Outline every Plasmodium parasite.
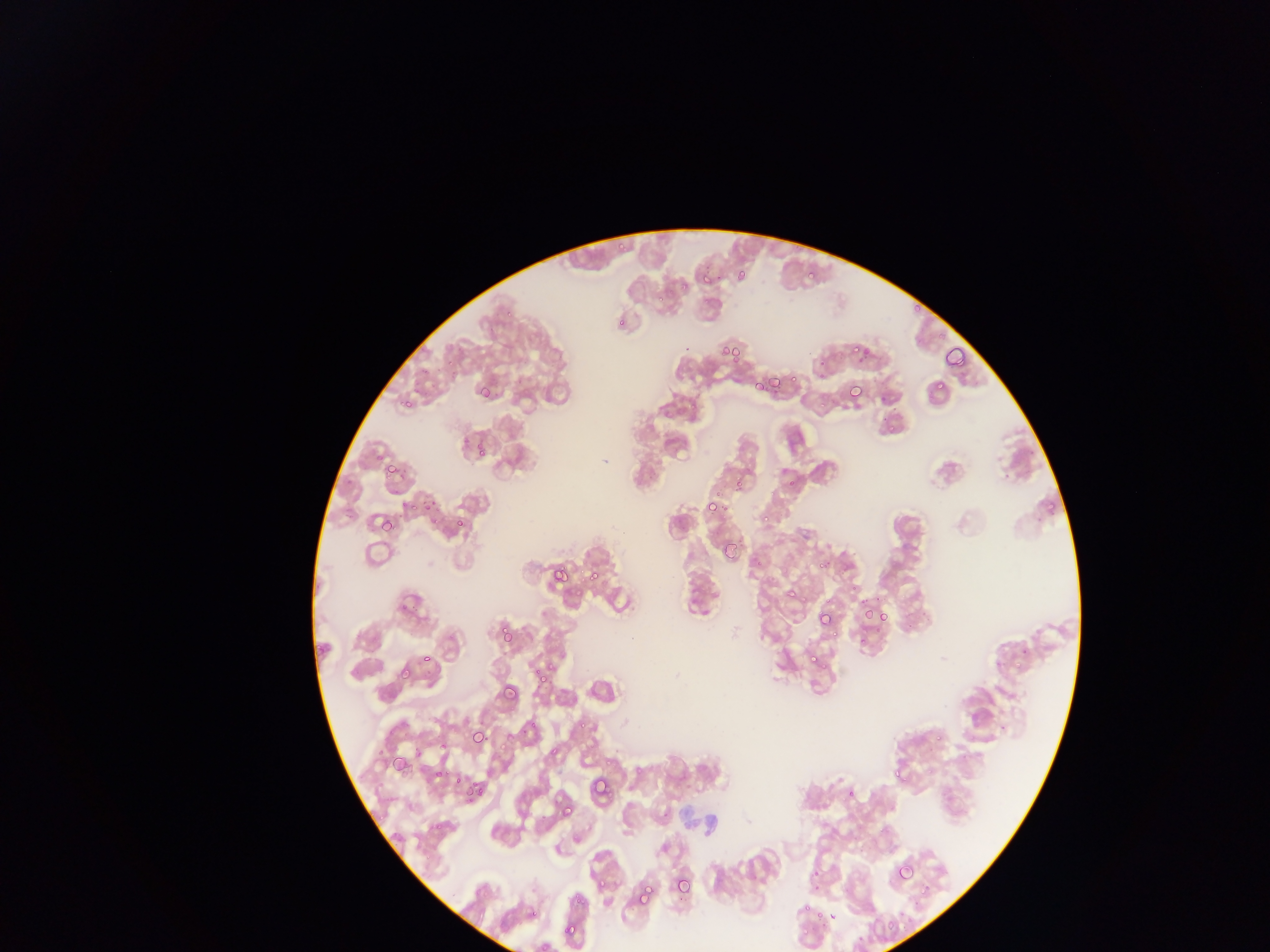
Approximate bounding boxes as (left, top, right, bottom) in pixels.
Plasmodium parasites: (615, 231, 636, 254), (804, 266, 821, 285), (702, 267, 715, 285), (734, 268, 753, 285), (669, 285, 679, 298), (904, 296, 921, 314), (614, 316, 623, 326), (716, 341, 739, 365), (942, 347, 965, 373), (843, 348, 869, 361), (931, 369, 948, 391), (767, 371, 790, 393), (748, 377, 760, 397), (477, 384, 497, 405), (839, 385, 864, 413), (402, 395, 415, 412), (472, 442, 488, 457), (381, 458, 400, 483), (733, 474, 745, 497), (760, 497, 777, 526), (702, 500, 718, 516), (422, 502, 441, 526), (420, 505, 455, 531), (427, 512, 445, 531), (379, 513, 391, 536), (450, 520, 470, 534), (723, 537, 740, 556), (807, 564, 830, 571), (550, 565, 571, 587), (585, 566, 602, 585), (781, 582, 795, 605), (863, 601, 886, 626), (870, 609, 888, 628), (816, 610, 835, 630), (498, 624, 515, 645), (419, 652, 436, 668), (808, 652, 826, 670), (398, 665, 415, 683), (535, 665, 555, 686), (501, 684, 520, 704), (497, 709, 533, 752), (574, 709, 597, 732), (917, 716, 942, 748), (468, 727, 489, 748), (550, 741, 563, 761), (386, 748, 410, 772), (891, 759, 910, 779), (429, 766, 440, 780), (451, 772, 468, 790), (588, 776, 613, 804), (466, 781, 494, 811), (848, 781, 862, 802), (559, 801, 576, 819), (805, 852, 818, 875), (893, 859, 916, 884), (670, 873, 693, 897), (587, 877, 607, 891), (919, 878, 932, 900), (635, 885, 656, 908), (569, 887, 585, 905), (797, 888, 833, 926), (529, 895, 540, 908), (880, 913, 898, 942), (562, 920, 580, 940), (798, 928, 809, 945).

Summary:
  - Field of view: single
  - Country: Ghana
  - Capture: mobile-phone photograph through a microscope
  - Image size: 1270×952 pixels
  - Preparation: thin blood smear